Give the extent of all Plasmodium falciparum-infected red blood cells.
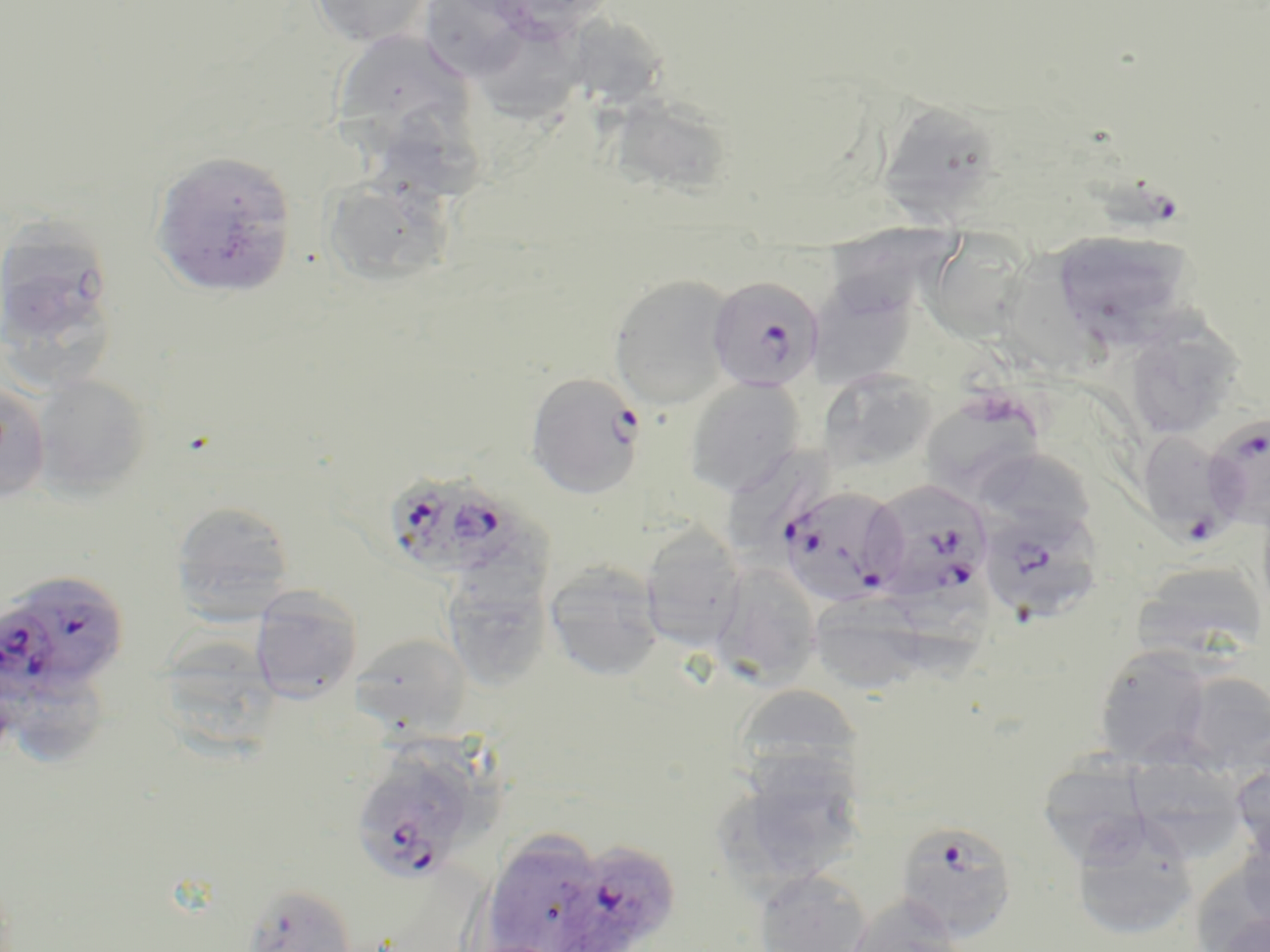
Approximate bounding boxes as (x1,y1)-(x2,y2) corner pairs in pixels.
Plasmodium falciparum-infected red blood cells (subset): (1088,165)-(1179,232), (707,275)-(824,393), (525,372)-(645,499), (1135,430)-(1241,541), (383,470)-(528,581), (864,478)-(994,605), (781,492)-(910,611), (976,501)-(1105,624), (11,577)-(127,683), (0,605)-(61,713), (351,754)-(477,884), (893,818)-(1019,942), (555,839)-(682,952).

{
  "slide_level_diagnosis": "Plasmodium falciparum",
  "preparation": "thin blood film",
  "uninfected_red_blood_cell_locations_subset": "approximate bounding boxes as (x1,y1)-(x2,y2) corner pairs in pixels: (308,0)-(435,48), (422,1)-(539,85), (568,15)-(669,107), (476,24)-(598,134), (331,28)-(477,157), (598,90)-(732,194), (873,97)-(1007,221), (390,104)-(487,202), (150,150)-(298,297), (323,173)-(454,288), (0,215)-(117,354), (827,218)-(954,317), (917,225)-(1039,340), (1050,228)-(1197,348), (996,251)-(1115,382), (608,273)-(737,409), (808,280)-(915,391), (1124,317)-(1243,441), (817,368)-(938,475), (31,374)-(152,501), (684,377)-(806,497), (0,380)-(50,503), (916,389)-(1048,503), (725,439)-(838,556), (974,447)-(1098,541), (171,500)-(295,624), (640,527)-(746,652), (712,561)-(822,687), (1134,561)-(1267,662), (544,563)-(664,681), (440,568)-(554,693), (889,572)-(994,691), (250,586)-(362,704), (808,591)-(930,694), (353,633)-(471,734), (166,638)-(281,758), (1092,646)-(1216,767), (1174,670)-(1270,776), (2,671)-(105,765), (733,684)-(864,785), (1133,739)-(1249,869), (1230,757)-(1270,869), (715,758)-(869,894), (1047,762)-(1154,862), (1069,818)-(1201,943), (1234,830)-(1270,936), (481,832)-(609,952), (752,868)-(873,952), (240,882)-(358,952), (845,894)-(968,952), (1210,913)-(1270,952)",
  "field_of_view": "single",
  "image_size": "1270×952 pixels",
  "stain": "May-Grünwald-Giemsa",
  "modality": "light microscopy",
  "magnification": "1000x"
}